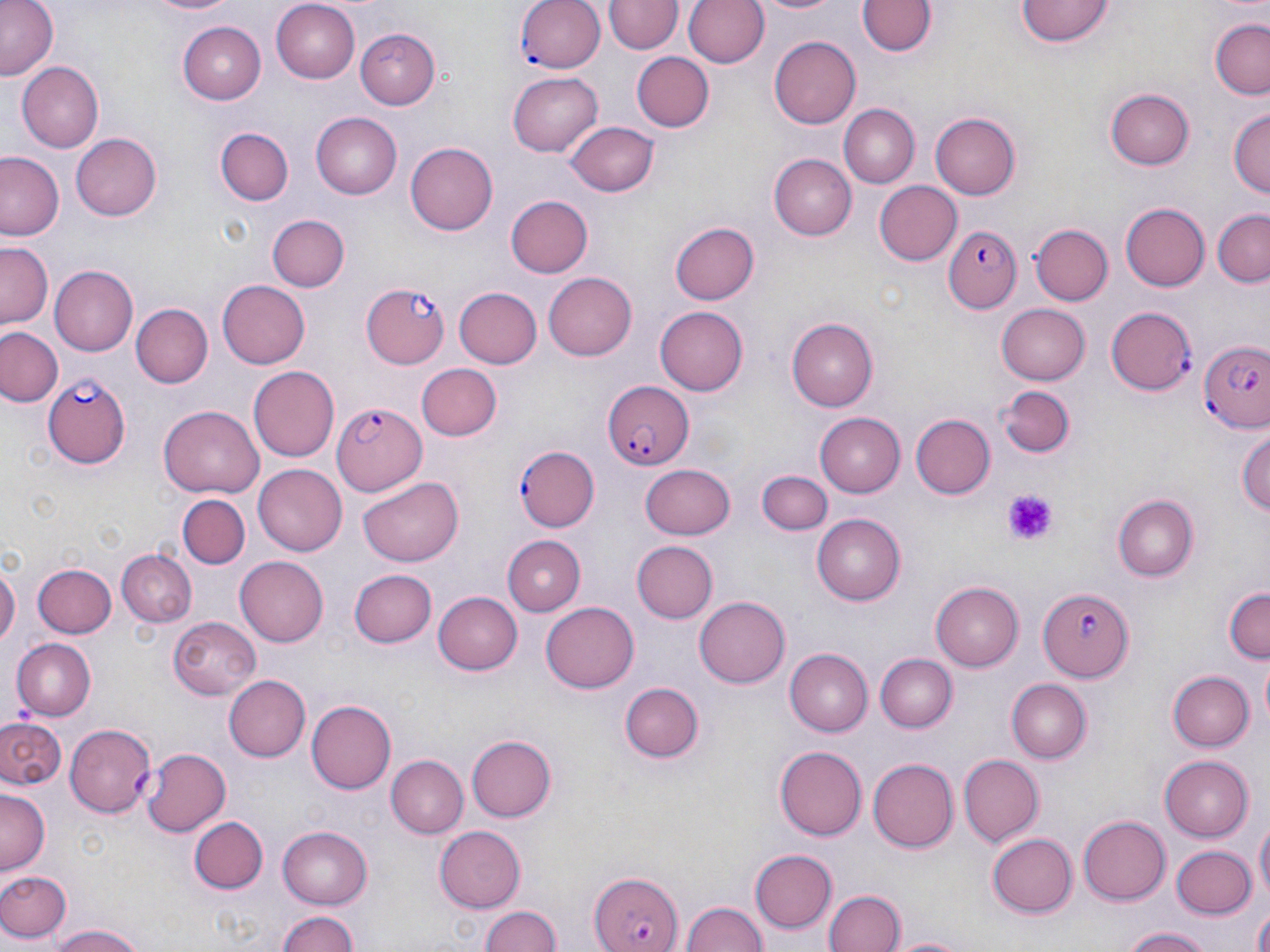
Summary:
  - Coordinate format: approximate bounding boxes as (x1, y1, x2, y2) in pixels
  - Uninfected red blood cell locations: (1, 0, 60, 79), (135, 0, 239, 16), (269, 0, 360, 84), (606, 0, 680, 55), (682, 0, 767, 70), (754, 0, 842, 16), (1019, 0, 1115, 48), (859, 1, 936, 57), (1209, 21, 1270, 99), (176, 22, 266, 104), (359, 29, 438, 109), (769, 36, 861, 129), (630, 52, 714, 132), (16, 62, 104, 153), (508, 73, 604, 156), (1106, 89, 1192, 170), (839, 105, 919, 188), (1228, 109, 1269, 202), (310, 112, 401, 199), (931, 113, 1022, 200), (566, 120, 657, 197), (216, 127, 292, 206), (72, 133, 162, 221), (405, 142, 496, 235), (1, 153, 65, 240), (772, 153, 856, 240), (874, 181, 962, 265), (504, 194, 591, 279), (1120, 202, 1210, 292), (1210, 210, 1270, 288), (267, 212, 349, 291), (671, 222, 759, 306), (1030, 225, 1113, 308), (2, 242, 54, 328), (47, 263, 137, 357), (544, 272, 638, 361), (216, 279, 310, 369), (453, 287, 542, 370), (131, 304, 212, 387), (996, 304, 1090, 386), (654, 307, 749, 396), (786, 318, 877, 411), (0, 325, 63, 407), (415, 362, 501, 442), (249, 365, 339, 459), (994, 384, 1074, 461), (159, 406, 264, 497), (817, 413, 906, 498), (912, 414, 994, 498), (1237, 422, 1270, 522), (642, 461, 735, 540), (253, 464, 347, 555), (762, 471, 831, 534), (358, 477, 464, 565), (178, 493, 250, 570), (1114, 495, 1198, 581), (811, 515, 907, 605), (503, 535, 585, 614), (630, 540, 718, 624), (119, 547, 196, 627), (0, 556, 19, 654), (234, 556, 328, 647), (33, 562, 116, 638), (349, 570, 435, 647), (931, 581, 1025, 670), (1222, 587, 1269, 666), (433, 589, 522, 675), (694, 597, 789, 688), (541, 602, 639, 693), (167, 616, 260, 700), (12, 638, 95, 719), (785, 649, 872, 735), (875, 652, 956, 731), (1167, 670, 1255, 752), (223, 675, 307, 761), (1006, 679, 1090, 762), (619, 680, 704, 763), (307, 699, 397, 794), (1, 717, 65, 789), (66, 723, 159, 815), (467, 733, 557, 822), (773, 746, 865, 840), (1159, 753, 1253, 842), (958, 754, 1042, 847), (387, 756, 466, 839), (867, 757, 958, 854), (0, 789, 48, 873), (189, 814, 268, 893), (1254, 814, 1269, 909), (1078, 817, 1170, 904), (434, 825, 527, 913), (277, 826, 371, 909), (987, 833, 1077, 917), (1170, 843, 1257, 919), (750, 849, 837, 933), (0, 868, 71, 945), (823, 890, 904, 952), (680, 899, 766, 952), (478, 906, 564, 952), (274, 908, 361, 952), (1250, 908, 1270, 952), (48, 921, 150, 952), (1120, 926, 1219, 952), (884, 934, 978, 952)
  - Platelet locations: (999, 491, 1055, 544)
  - Plasmodium falciparum-infected red blood cell locations: (515, 0, 606, 74), (944, 223, 1020, 313), (360, 283, 451, 370), (1106, 306, 1195, 394), (1197, 340, 1270, 434), (44, 374, 131, 468), (601, 380, 694, 472), (330, 398, 425, 495), (516, 447, 599, 531), (1038, 587, 1135, 682), (129, 746, 229, 836), (589, 870, 683, 952)
  - Slide-level diagnosis: Plasmodium falciparum
  - Image size: 1270×952 pixels
  - Modality: light microscopy
  - Stain: May-Grünwald-Giemsa
  - Preparation: thin blood smear
  - Field of view: one of a larger specimen
  - Magnification: 1000x